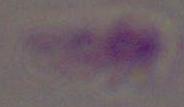
Summary:
  - Modality: micrograph
  - Magnification: 1000x
  - Identification: Toxoplasma gondii